Locate and identify every blood parasite.
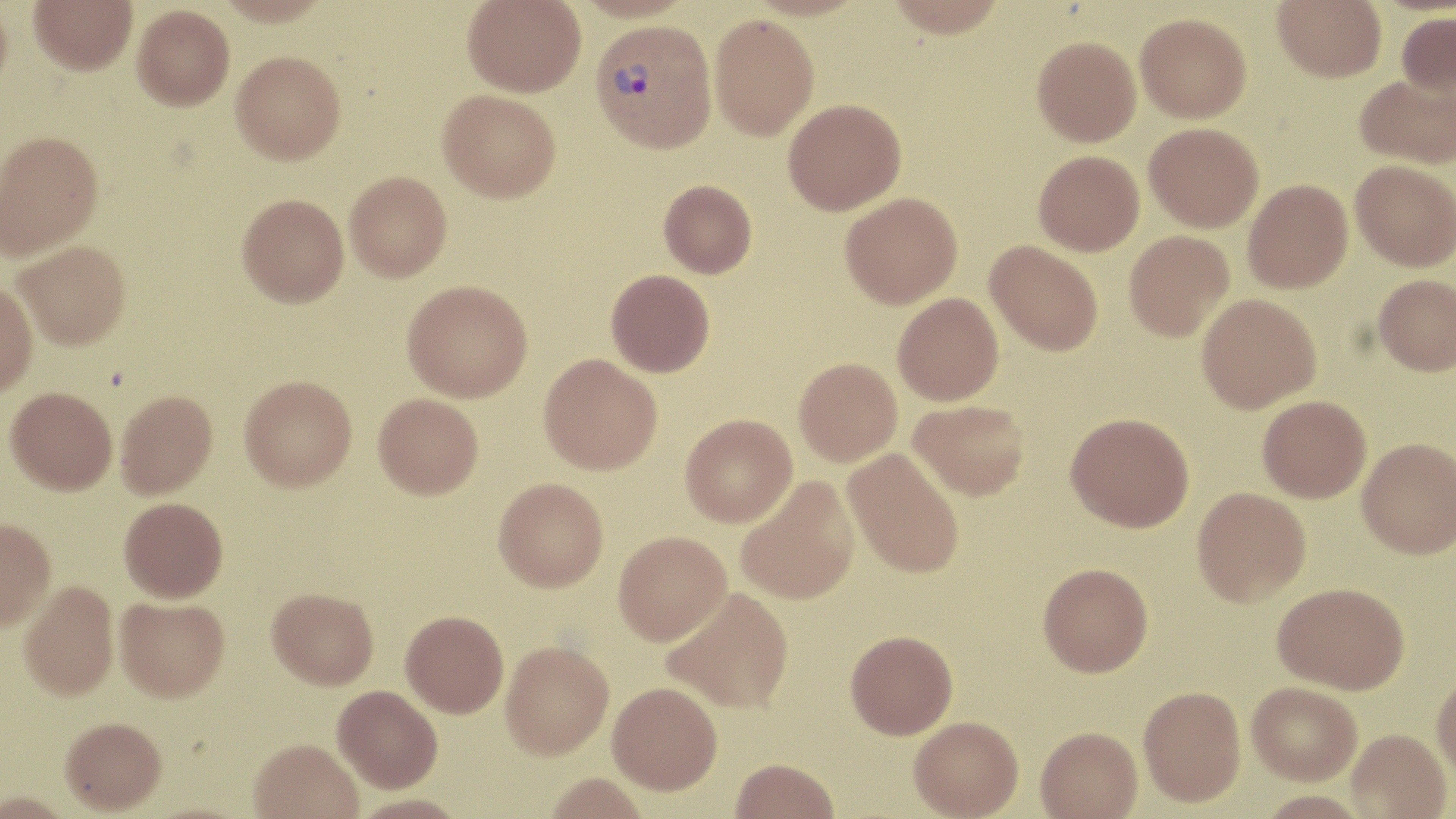

Approximate bounding boxes as [x1, y1, x2, y2] in pixels.
Plasmodium vivax-infected red blood cells: [590, 19, 717, 154].
No Plasmodium falciparum, Plasmodium ovale, Plasmodium malariae, Babesia divergens, or Trypanosoma brucei observed.

Summary:
  - Uninfected red blood cell locations: [0, 0, 13, 100], [29, 0, 137, 74], [214, 0, 333, 26], [462, 0, 585, 97], [571, 0, 698, 23], [883, 0, 1009, 38], [1273, 0, 1386, 82], [132, 4, 234, 110], [1395, 11, 1456, 98], [1135, 12, 1252, 122], [709, 14, 819, 140], [1032, 36, 1141, 147], [231, 50, 346, 164], [1355, 73, 1455, 169], [438, 89, 561, 203], [783, 99, 906, 215], [1144, 122, 1263, 232], [0, 130, 103, 259], [1033, 150, 1144, 255], [1350, 160, 1456, 271], [344, 171, 452, 282], [658, 179, 757, 278], [1243, 179, 1353, 293], [840, 192, 962, 308], [237, 194, 349, 306], [1124, 230, 1234, 341], [14, 240, 131, 349], [985, 241, 1103, 356], [606, 269, 715, 377], [1374, 274, 1456, 376], [0, 279, 38, 398], [402, 280, 532, 402], [893, 292, 1004, 406], [1196, 293, 1321, 413], [538, 353, 663, 474], [794, 357, 903, 466], [239, 375, 356, 490], [5, 387, 117, 494], [115, 390, 217, 499], [373, 393, 483, 499], [1258, 395, 1371, 503], [908, 399, 1030, 501], [1065, 412, 1194, 532], [680, 414, 797, 527], [1357, 437, 1456, 558], [842, 449, 965, 578], [735, 475, 860, 605], [493, 477, 608, 591], [1191, 486, 1311, 607], [119, 497, 228, 602], [0, 518, 56, 631], [613, 530, 731, 645], [1038, 562, 1153, 676], [18, 581, 120, 700], [1273, 582, 1409, 695], [662, 587, 794, 714], [267, 588, 378, 689], [115, 596, 230, 701], [401, 610, 508, 717], [846, 630, 958, 738], [500, 640, 614, 759], [1432, 669, 1456, 782], [607, 681, 723, 794], [1246, 682, 1362, 785], [332, 685, 443, 793], [1138, 685, 1245, 806], [909, 716, 1024, 818], [60, 718, 167, 816], [1036, 726, 1142, 818], [1347, 728, 1451, 818], [249, 738, 363, 819], [730, 758, 840, 819], [543, 774, 650, 818], [0, 794, 75, 819]
  - Slide-level diagnosis: Plasmodium vivax
  - Preparation: thin blood smear
  - Field of view: one of a larger specimen
  - Image size: 1456×819 pixels
  - Stain: May-Grünwald-Giemsa
  - Magnification: 1000x
  - Modality: optical microscopy